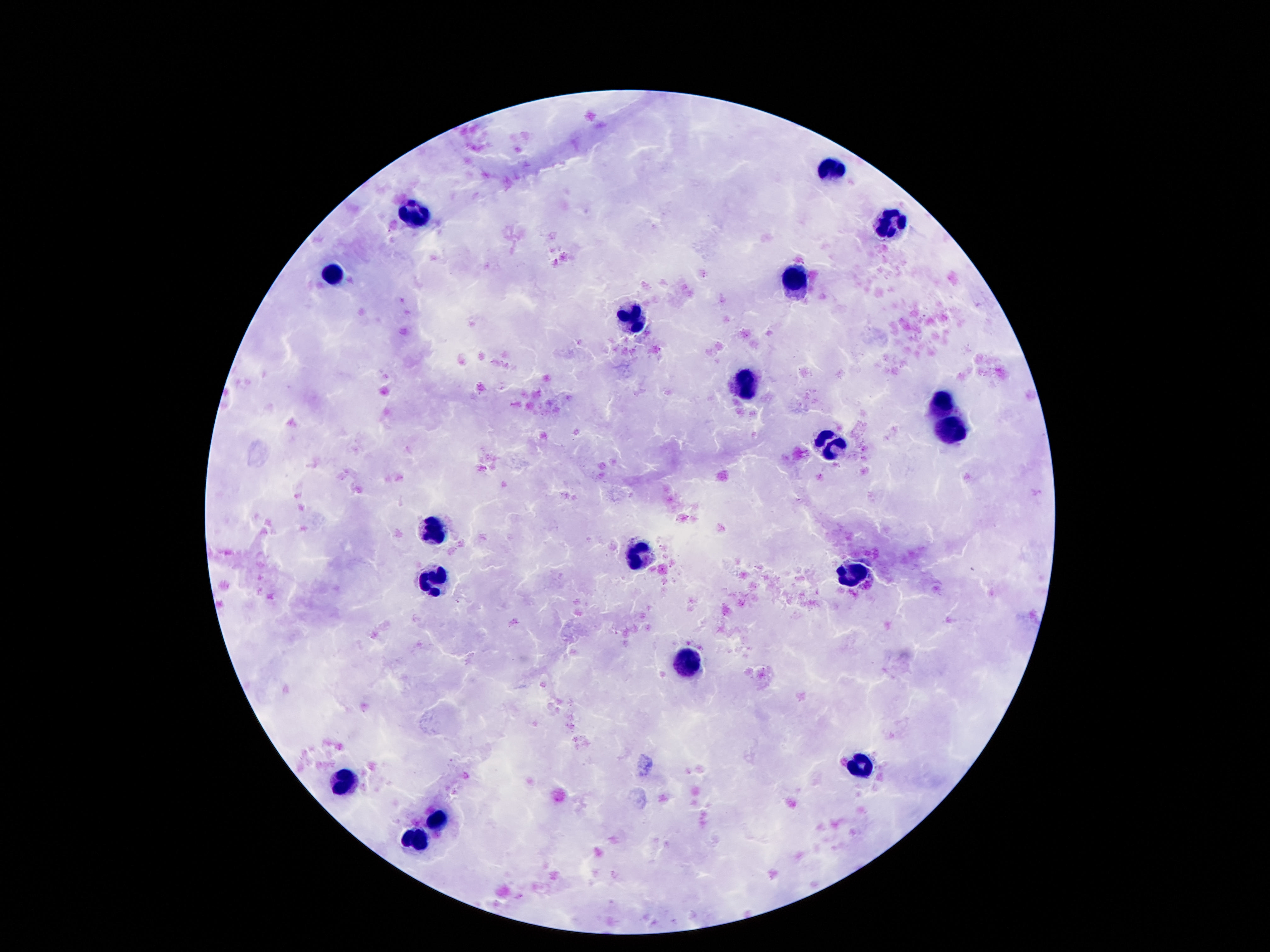
patient malaria status = uninfected
field of view = one from this slide
stain = Giemsa
image size = 1270×952 pixels
capture = smartphone camera through the microscope eyepiece
magnification = 100x
leukocyte locations = approximate centers as (x, y) in pixels: (827, 168), (416, 212), (892, 223), (338, 275), (798, 281), (632, 318), (745, 384), (942, 402), (953, 429), (829, 445), (435, 524), (640, 555), (858, 573), (434, 575), (688, 661), (861, 766), (346, 779), (437, 820), (418, 838)
preparation = thick blood smear